Assess this cell for malaria.
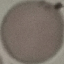

It is uninfected.

Summary:
  - Image type: automatically extracted cell patch, resized to 64 × 64 pixels
  - Preparation: thin blood smear
  - Capture: smartphone through the microscope eyepiece
  - Stain: Giemsa